Name the parasite shown.
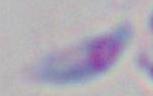
Toxoplasma gondii.

magnification = 1000x
modality = micrograph